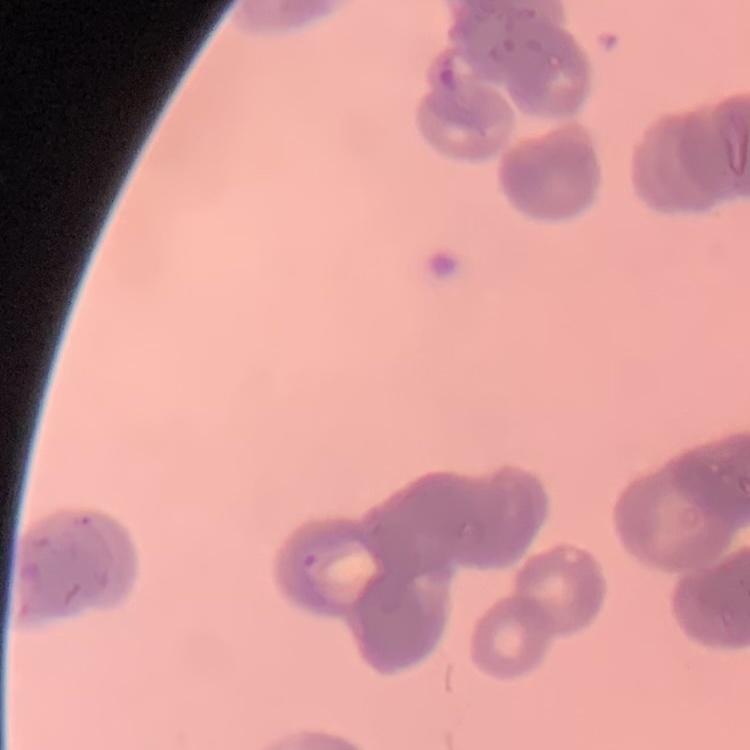

Summary:
  - Erythrocyte morphology: rouleaux formation
  - Preparation: thin blood film
  - Image type: one tile cut from a larger photomicrograph
  - Stain: Field's or Giemsa